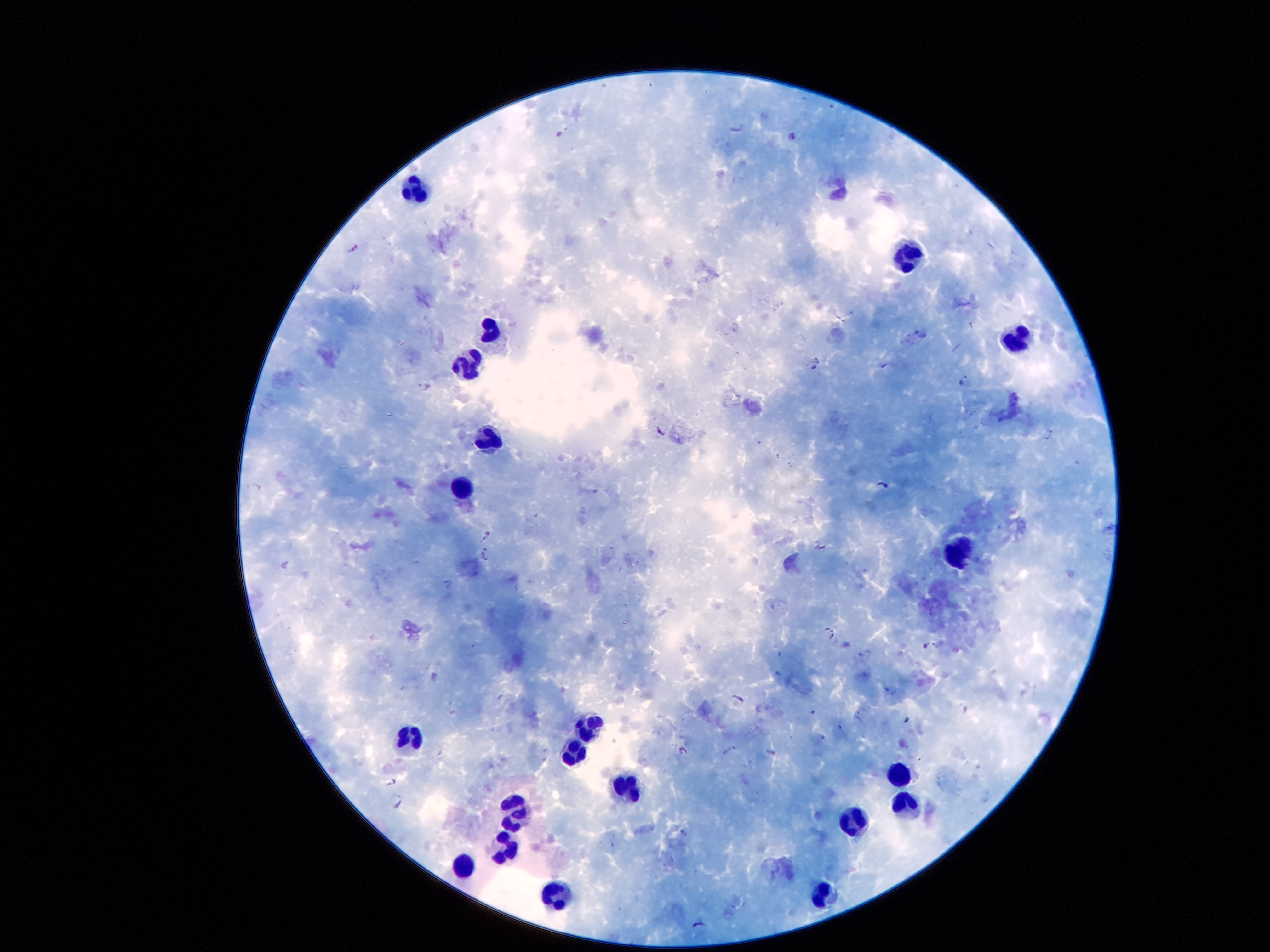
Approximate centers as {x, y} in pixels. Plasmodium parasite locations: {792, 136}, {354, 248}, {818, 360}, {813, 368}, {964, 379}, {425, 387}, {661, 431}, {883, 487}, {485, 536}, {486, 556}, {284, 563}, {830, 633}, {924, 645}, {739, 698}, {728, 750}, {683, 751}, {771, 752}, {394, 783}, {397, 803}. Leukocyte locations: {416, 189}, {908, 257}, {490, 332}, {1021, 344}, {470, 368}, {486, 439}, {463, 493}, {962, 554}, {590, 727}, {415, 739}, {568, 751}, {897, 777}, {624, 790}, {908, 804}, {518, 815}, {853, 823}, {506, 854}, {465, 868}, {819, 893}, {554, 900}. Smartphone photograph taken through the microscope eyepiece. Thick blood smear. Giemsa stain. Image is 1270×952 pixels. One field from this slide. Patient malaria status: infected with Plasmodium falciparum. 100x magnification.